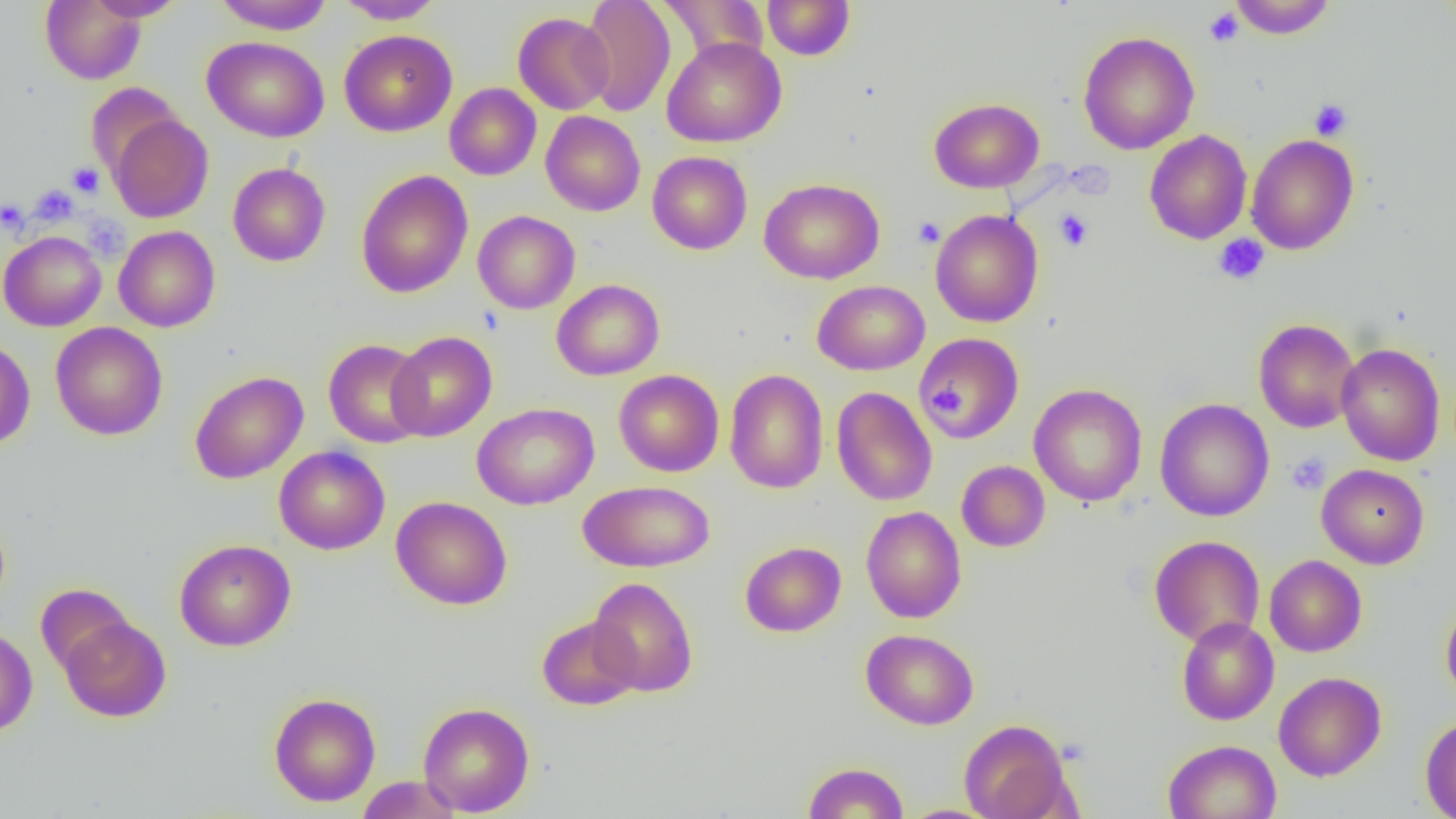
{
  "slide_level_diagnosis": "negative for blood parasites",
  "modality": "optical microscopy",
  "platelet_locations": "approximate bounding boxes as (x1, y1, x2, y2) in pixels: (1204, 7, 1243, 46), (1309, 99, 1353, 141), (67, 162, 104, 198), (29, 185, 80, 225), (1, 198, 29, 234), (1055, 208, 1093, 251), (913, 217, 945, 248), (1213, 234, 1269, 285), (931, 385, 964, 418), (1286, 452, 1331, 494)",
  "image_size": "1456×819 pixels",
  "uninfected_red_blood_cell_locations": "approximate bounding boxes as (x1, y1, x2, y2) in pixels: (40, 0, 146, 84), (84, 0, 187, 21), (212, 0, 334, 34), (335, 0, 445, 24), (579, 0, 676, 116), (658, 0, 769, 65), (762, 0, 855, 60), (1229, 0, 1336, 39), (513, 12, 614, 115), (339, 30, 457, 137), (1078, 31, 1199, 154), (202, 36, 330, 142), (661, 37, 787, 148), (85, 81, 185, 180), (444, 83, 541, 180), (929, 98, 1044, 192), (540, 111, 645, 216), (107, 113, 213, 223), (1145, 130, 1252, 244), (1245, 134, 1359, 255), (647, 151, 753, 254), (227, 162, 330, 267), (356, 170, 473, 298), (759, 178, 885, 284), (930, 209, 1043, 327), (473, 210, 580, 314), (114, 225, 220, 332), (0, 230, 106, 331), (552, 279, 665, 380), (813, 281, 930, 375), (1253, 318, 1360, 433), (50, 322, 168, 440), (387, 331, 497, 442), (915, 333, 1024, 444), (0, 337, 35, 450), (323, 339, 430, 447), (1336, 342, 1445, 466), (614, 369, 724, 477), (724, 369, 829, 494), (189, 370, 308, 484), (1029, 383, 1147, 507), (832, 386, 937, 506), (1155, 398, 1274, 522), (472, 402, 599, 510), (274, 445, 390, 555), (956, 460, 1050, 552), (1316, 464, 1429, 569), (578, 480, 715, 573), (392, 496, 512, 610), (861, 506, 966, 623), (1149, 535, 1265, 647), (174, 539, 296, 652), (740, 541, 846, 637), (1264, 555, 1367, 657), (588, 577, 698, 697), (36, 583, 135, 677), (1441, 599, 1456, 706), (537, 615, 641, 711), (59, 616, 171, 722), (1176, 617, 1279, 725), (0, 628, 38, 736), (861, 628, 979, 729), (1274, 672, 1386, 781), (269, 692, 380, 807), (418, 702, 535, 816), (1420, 716, 1456, 819), (959, 718, 1075, 819), (1163, 739, 1281, 819), (802, 762, 909, 819), (356, 776, 462, 819), (896, 805, 1001, 819)",
  "field_of_view": "single",
  "magnification": "1000x",
  "preparation": "thin blood smear"
}